Identify the cell.
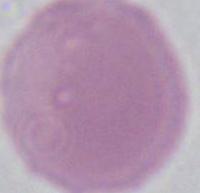
This is an erythrocyte.

modality = micrograph
magnification = 1000x